Classify this cell by malaria status.
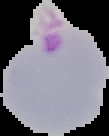
It is parasitized.

Segmented cell region on a black background. From a thin blood smear. Image is 109×136 pixels.